Identify the blood parasite species.
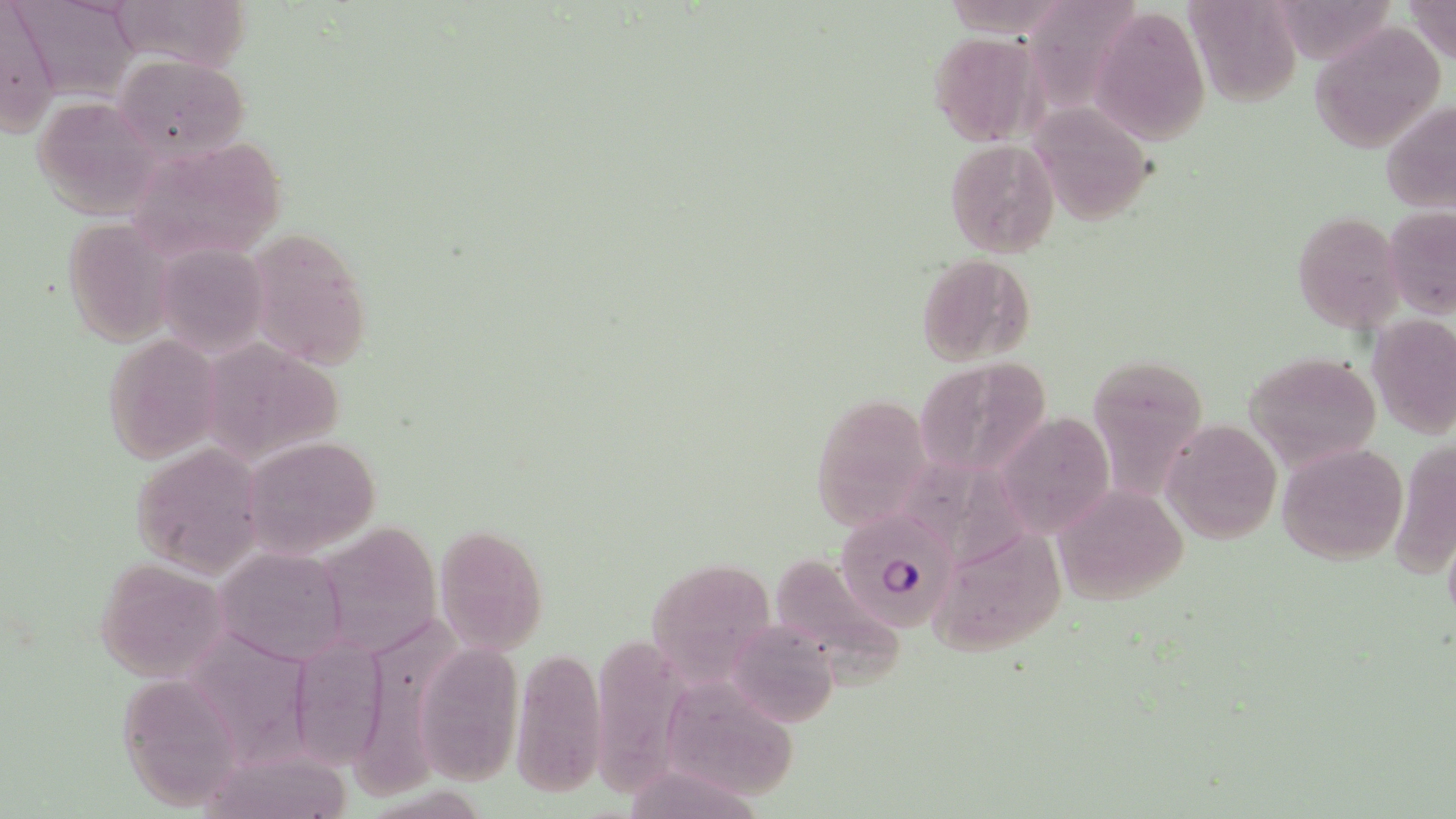

Plasmodium falciparum.

uninfected red blood cell locations = approximate bounding boxes as (x1,y1)-(x2,y2) corner pairs in pixels: (105,0)-(254,71), (1027,0)-(1146,122), (1402,0)-(1456,67), (1,1)-(60,136), (12,1)-(141,95), (1184,1)-(1304,107), (1091,4)-(1212,143), (1308,21)-(1445,154), (927,30)-(1042,146), (113,54)-(248,162), (32,95)-(165,219), (1382,100)-(1456,215), (1031,101)-(1155,225), (124,136)-(289,262), (945,138)-(1062,258), (1382,204)-(1456,320), (1293,209)-(1406,334), (61,216)-(180,348), (243,228)-(376,368), (153,242)-(270,358), (914,254)-(1036,364), (1368,316)-(1456,440), (103,334)-(225,465), (201,343)-(357,465), (1246,350)-(1383,470), (1102,354)-(1201,520), (916,360)-(1052,491), (812,392)-(933,527), (997,412)-(1114,539), (1161,419)-(1282,544), (246,435)-(382,555), (1389,437)-(1456,581), (1276,441)-(1408,565), (132,442)-(266,577), (1052,485)-(1188,605), (330,512)-(448,665), (436,528)-(548,655), (940,539)-(1075,664), (213,546)-(351,665), (95,557)-(232,681), (782,560)-(908,696), (639,566)-(779,688), (363,615)-(472,796), (729,617)-(839,729), (185,629)-(314,778), (583,631)-(685,796), (298,633)-(399,786), (411,642)-(524,786), (510,647)-(606,795), (117,676)-(248,803), (669,684)-(815,804), (200,753)-(371,819)
image size = 1456×819 pixels
field of view = single
Plasmodium falciparum-infected red blood cell locations = approximate bounding boxes as (x1,y1)-(x2,y2) corner pairs in pixels: (837,505)-(959,634)
preparation = thin blood film
magnification = 1000x
stain = May-Grünwald-Giemsa
modality = optical microscopy